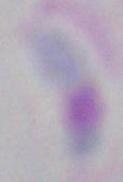 1000x magnification. Toxoplasma gondii is shown. Photomicrograph.